Comment on the morphology of the erythrocytes.
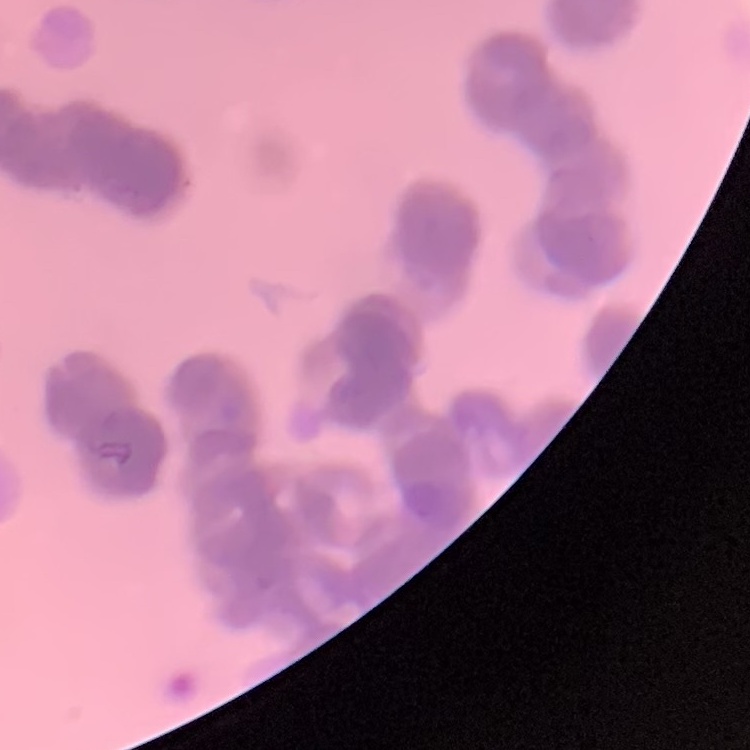
Rouleaux formation.

{
  "image_type": "square crop of a larger photomicrograph",
  "stain": "Field's or Giemsa",
  "preparation": "thin blood smear"
}